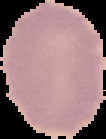 Malaria status: uninfected. Image is 106×139 pixels. From a thin blood smear. Cell region segmented out of the field of view; the surrounding area is masked to black.